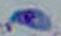

magnification = 1000x
modality = micrograph
identification = Toxoplasma gondii